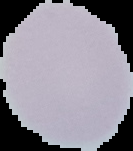
{
  "result": "no Plasmodium parasites seen",
  "preparation": "thin blood film",
  "image_size": "133×151 pixels",
  "image_type": "cell region segmented out of the field of view; surrounding area masked to black"
}